Assess this cell for malaria.
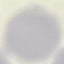

Uninfected.

Automatically extracted cell patch, resized to 64 × 64 pixels. Acquired by smartphone through the microscope eyepiece. Giemsa stain. Thin blood smear.